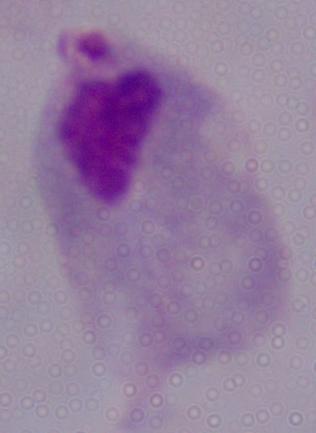

Summary:
  - Magnification: 1000x
  - Modality: micrograph
  - Identification: trichomonad